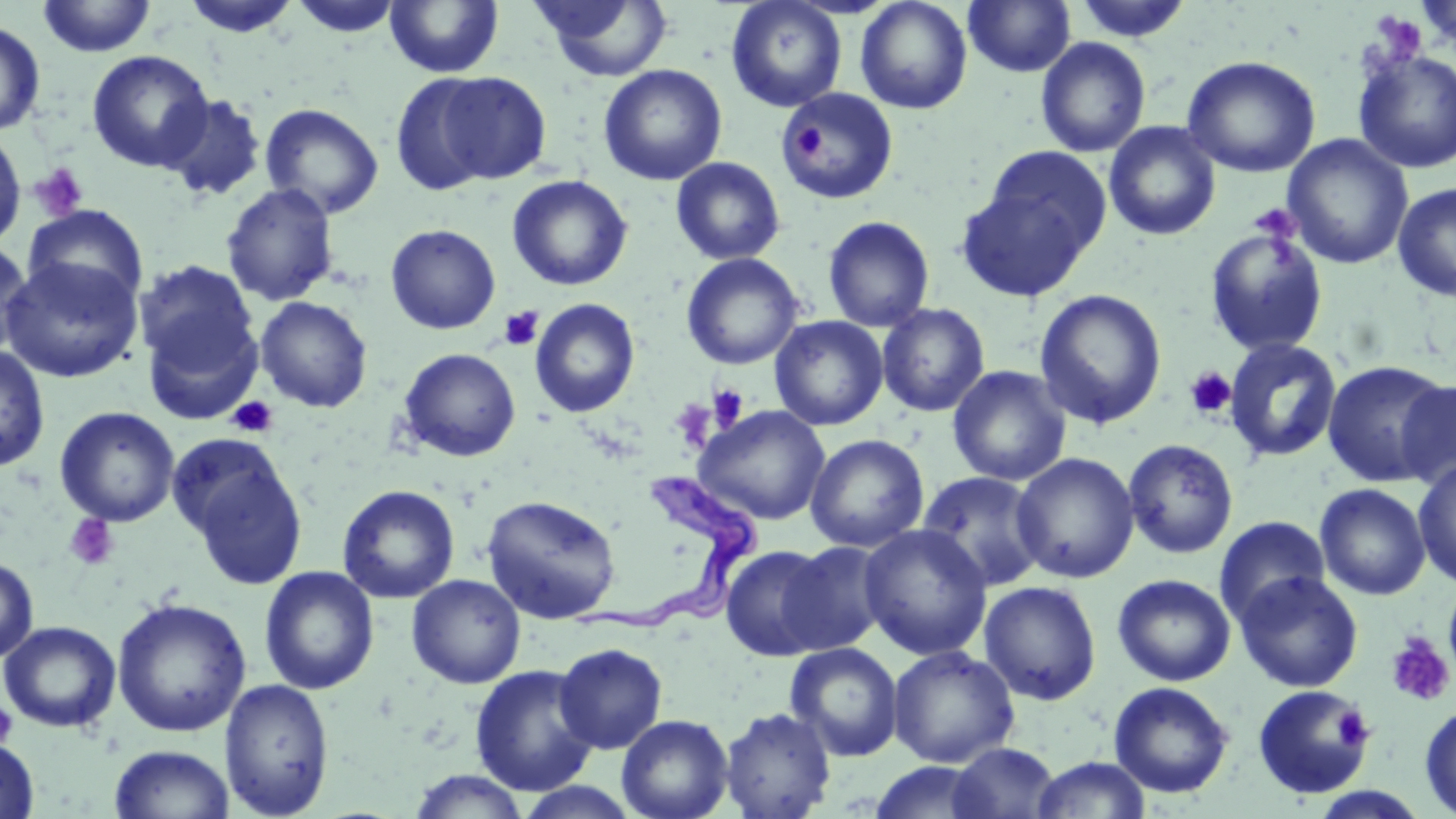

{
  "slide_level_diagnosis": "Trypanosoma brucei",
  "platelet_locations": "approximate bounding boxes as (x1, y1, x2, y2) in pixels: (1372, 13, 1428, 64), (789, 126, 826, 160), (29, 162, 90, 221), (1249, 204, 1301, 243), (497, 306, 544, 351), (1185, 366, 1236, 419), (707, 383, 749, 428), (227, 396, 279, 438), (671, 399, 717, 449), (63, 513, 120, 571), (1385, 632, 1455, 706), (0, 701, 18, 749), (1331, 706, 1373, 749)",
  "uninfected_red_blood_cell_locations": "approximate bounding boxes as (x1, y1, x2, y2) in pixels: (37, 0, 157, 58), (180, 0, 302, 38), (288, 0, 406, 37), (725, 0, 848, 113), (855, 0, 973, 114), (964, 0, 1076, 77), (1071, 0, 1194, 44), (384, 1, 504, 78), (530, 1, 675, 82), (1415, 1, 1456, 53), (0, 20, 46, 137), (1035, 37, 1151, 158), (1352, 49, 1456, 174), (86, 50, 215, 172), (1181, 55, 1321, 178), (598, 64, 727, 186), (433, 71, 551, 185), (388, 73, 500, 196), (778, 88, 898, 204), (160, 94, 267, 202), (260, 103, 384, 219), (1104, 121, 1221, 240), (0, 127, 26, 252), (1282, 134, 1414, 270), (981, 145, 1112, 263), (670, 157, 786, 265), (507, 175, 632, 291), (954, 179, 1092, 300), (1393, 182, 1456, 303), (221, 183, 340, 307), (23, 204, 149, 309), (823, 216, 935, 331), (385, 224, 501, 335), (1204, 227, 1329, 357), (0, 238, 35, 361), (681, 253, 803, 370), (1, 257, 143, 383), (134, 259, 260, 379), (1034, 288, 1168, 430), (255, 296, 373, 413), (530, 298, 640, 418), (877, 302, 990, 417), (770, 316, 888, 431), (1224, 337, 1342, 464), (0, 345, 51, 474), (398, 348, 521, 462), (1321, 360, 1452, 487), (948, 366, 1071, 486), (1395, 379, 1456, 491), (54, 406, 180, 527), (694, 406, 831, 524), (805, 434, 929, 552), (1122, 438, 1239, 559), (172, 439, 308, 590), (1011, 453, 1140, 583), (1413, 460, 1456, 588), (916, 471, 1049, 592), (1315, 483, 1431, 600), (337, 484, 460, 603), (481, 494, 622, 624), (1214, 516, 1329, 625), (858, 524, 993, 660), (780, 541, 892, 654), (719, 544, 835, 661), (0, 556, 39, 664), (259, 566, 379, 694), (1234, 571, 1364, 692), (406, 574, 526, 688), (1113, 574, 1236, 686), (979, 580, 1102, 705), (1443, 583, 1456, 679), (111, 598, 251, 737), (0, 620, 122, 733), (554, 642, 668, 754), (785, 643, 903, 761), (887, 645, 1020, 768), (470, 664, 599, 797), (219, 678, 335, 818), (1108, 681, 1234, 798), (1252, 685, 1374, 799), (1419, 703, 1456, 817), (719, 706, 836, 819), (616, 714, 734, 819), (0, 738, 40, 818), (947, 742, 1060, 819), (109, 745, 235, 819), (1030, 756, 1151, 818), (869, 761, 993, 818), (406, 769, 530, 819), (1308, 787, 1431, 819)",
  "image_size": "1456×819 pixels",
  "magnification": "1000x",
  "field_of_view": "one of a larger specimen",
  "trypanosoma_brucei_locations": "approximate bounding boxes as (x1, y1, x2, y2) in pixels: (561, 472, 764, 640)",
  "preparation": "thin blood film",
  "stain": "May-Grünwald-Giemsa",
  "modality": "light microscopy"
}